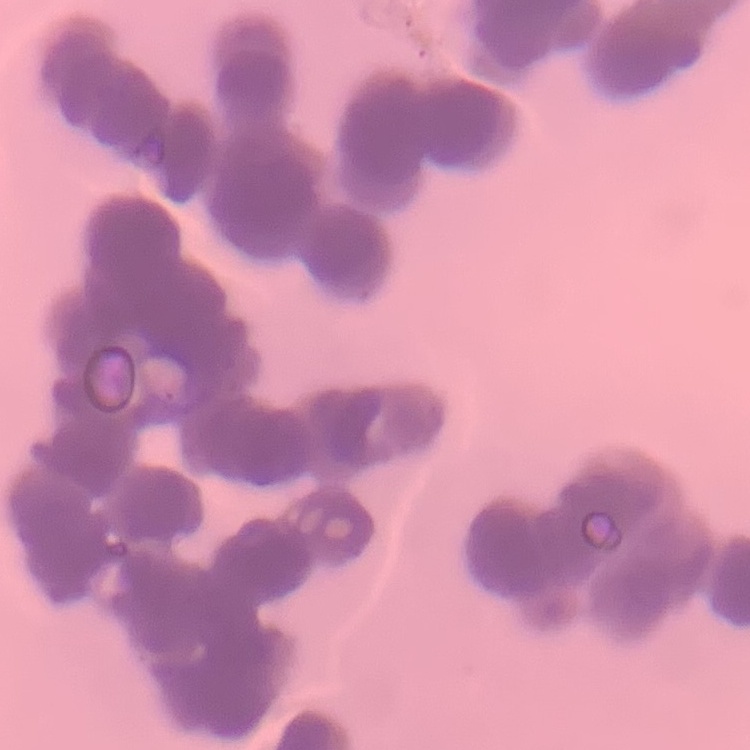
The red blood cells exhibit rouleaux formation. Thin blood film. One tile cut from a larger photomicrograph. Stained with either Field's or Giemsa.